Classify this cell by malaria status.
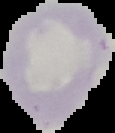

Uninfected.

Cell region segmented out of the field of view; the surrounding area is masked to black. From a thin blood film. Image is 115×133 pixels.